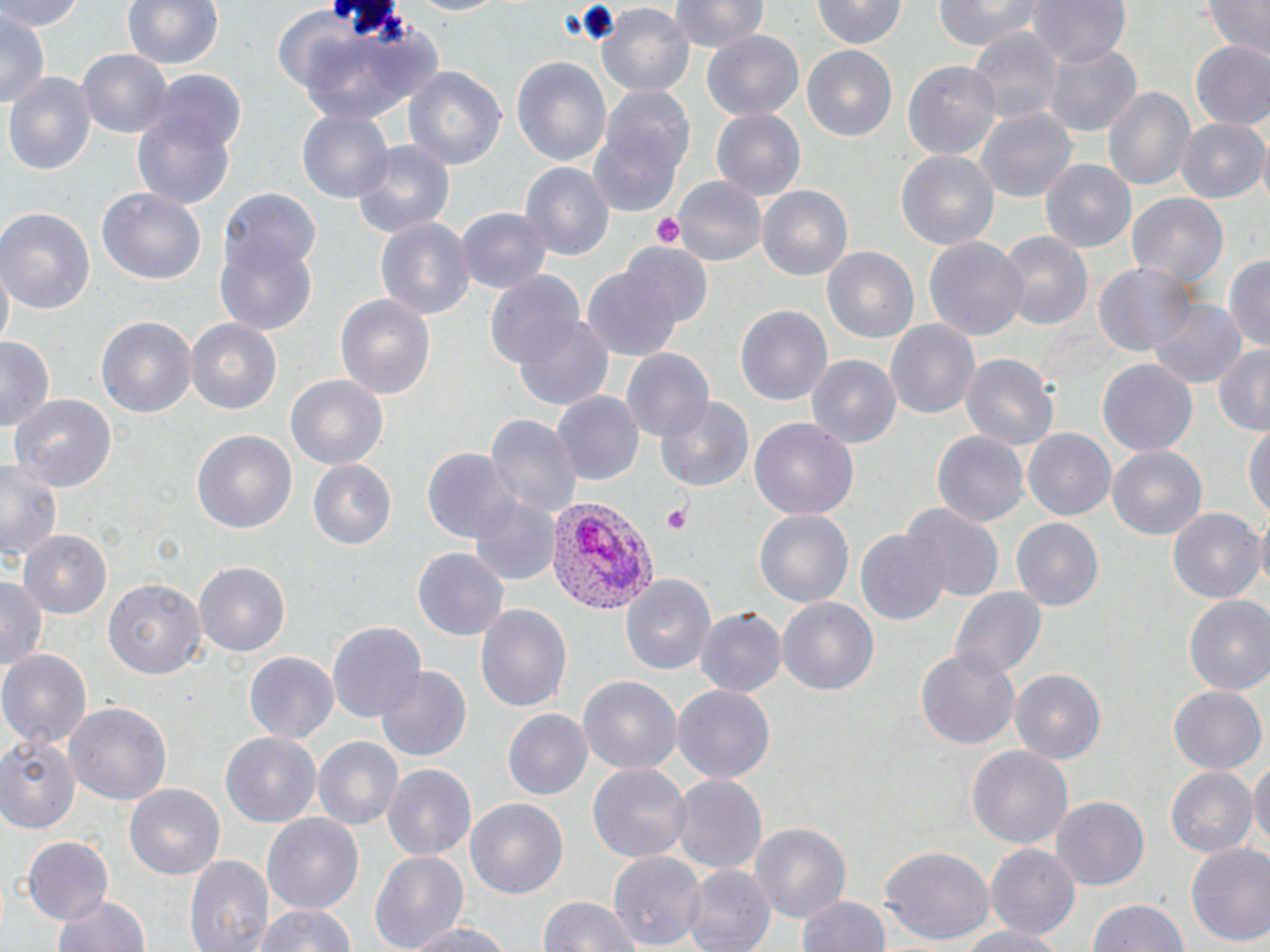

{
  "slide_level_diagnosis": "Plasmodium vivax",
  "uninfected_red_blood_cell_locations": "approximate bounding boxes as (x1,y1)-(x2,y2) corner pairs in pixels: (0,0)-(89,32), (124,0)-(223,70), (396,0)-(510,18), (669,0)-(773,54), (931,0)-(1042,52), (1023,0)-(1130,71), (1204,0)-(1269,59), (595,1)-(696,98), (811,1)-(905,50), (949,4)-(1051,90), (286,9)-(444,126), (0,11)-(47,113), (965,23)-(1064,126), (702,31)-(803,121), (1041,38)-(1140,138), (1188,41)-(1270,130), (801,43)-(898,139), (74,47)-(174,140), (511,57)-(611,167), (901,57)-(1003,159), (403,67)-(505,174), (4,71)-(96,174), (146,71)-(248,156), (1103,84)-(1196,196), (590,86)-(693,216), (975,107)-(1075,205), (709,108)-(806,200), (295,110)-(395,203), (134,114)-(234,208), (1176,117)-(1267,203), (349,140)-(455,238), (896,150)-(1000,254), (1040,157)-(1136,250), (519,162)-(613,262), (673,176)-(767,266), (757,186)-(852,284), (221,187)-(319,274), (97,188)-(204,285), (1125,192)-(1229,293), (455,206)-(551,296), (0,207)-(94,313), (218,217)-(319,333), (374,218)-(474,319), (995,231)-(1093,333), (925,235)-(1029,340), (623,242)-(713,328), (821,246)-(920,347), (1226,253)-(1270,351), (1094,262)-(1196,356), (579,265)-(685,363), (485,272)-(587,372), (334,293)-(435,403), (1147,297)-(1245,390), (736,305)-(831,405), (514,312)-(616,413), (97,316)-(197,418), (184,317)-(282,413), (884,319)-(981,420), (0,335)-(56,431), (1211,345)-(1270,436), (622,349)-(711,440), (960,351)-(1058,451), (807,355)-(900,448), (1099,360)-(1196,457), (287,375)-(387,472), (550,391)-(643,486), (8,394)-(118,494), (657,396)-(753,493), (485,414)-(581,518), (1245,417)-(1269,528), (749,419)-(858,521), (931,428)-(1029,528), (1024,428)-(1116,521), (192,430)-(297,535), (1107,447)-(1205,540), (422,449)-(515,543), (0,456)-(64,563), (307,459)-(397,549), (468,492)-(561,585), (901,501)-(1005,601), (1167,505)-(1263,601), (754,510)-(852,608), (1255,511)-(1270,597), (1012,517)-(1102,609), (856,526)-(949,627), (19,529)-(113,620), (414,546)-(510,641), (196,563)-(291,656), (0,573)-(47,674), (622,573)-(717,672), (104,575)-(204,679), (951,588)-(1046,680), (1183,595)-(1270,698), (777,597)-(879,699), (477,603)-(572,716), (693,608)-(784,697), (326,620)-(426,726), (916,648)-(1021,749), (0,649)-(92,750), (245,649)-(340,741), (374,662)-(470,762), (1010,668)-(1106,763), (577,676)-(682,777), (673,685)-(775,784), (1168,685)-(1266,776), (65,702)-(172,806), (502,709)-(592,800), (221,732)-(320,826), (1,735)-(81,834), (312,738)-(402,831), (967,743)-(1074,850), (1249,756)-(1270,857), (587,762)-(691,863), (382,763)-(476,861), (1164,765)-(1255,859), (670,774)-(767,874), (125,782)-(227,881), (1052,796)-(1148,889), (464,797)-(568,902), (262,813)-(366,917), (749,820)-(852,923), (22,836)-(114,928), (1184,841)-(1270,950), (985,844)-(1082,939), (880,846)-(993,945), (369,850)-(469,952), (185,851)-(275,952), (609,852)-(707,948), (682,864)-(775,952), (798,892)-(891,952), (52,894)-(152,952), (538,896)-(640,952), (1086,898)-(1189,952), (252,901)-(356,952), (401,919)-(513,951), (951,924)-(1070,952)",
  "stain": "May-Grünwald-Giemsa",
  "platelet_locations": "approximate bounding boxes as (x1,y1)-(x2,y2) corner pairs in pixels: (654,212)-(685,249), (663,503)-(693,535)",
  "image_size": "1270×952 pixels",
  "preparation": "thin blood smear",
  "modality": "optical microscopy",
  "field_of_view": "single",
  "plasmodium_vivax_infected_red_blood_cell_locations": "approximate bounding boxes as (x1,y1)-(x2,y2) corner pairs in pixels: (546,494)-(657,618)",
  "magnification": "1000x"
}